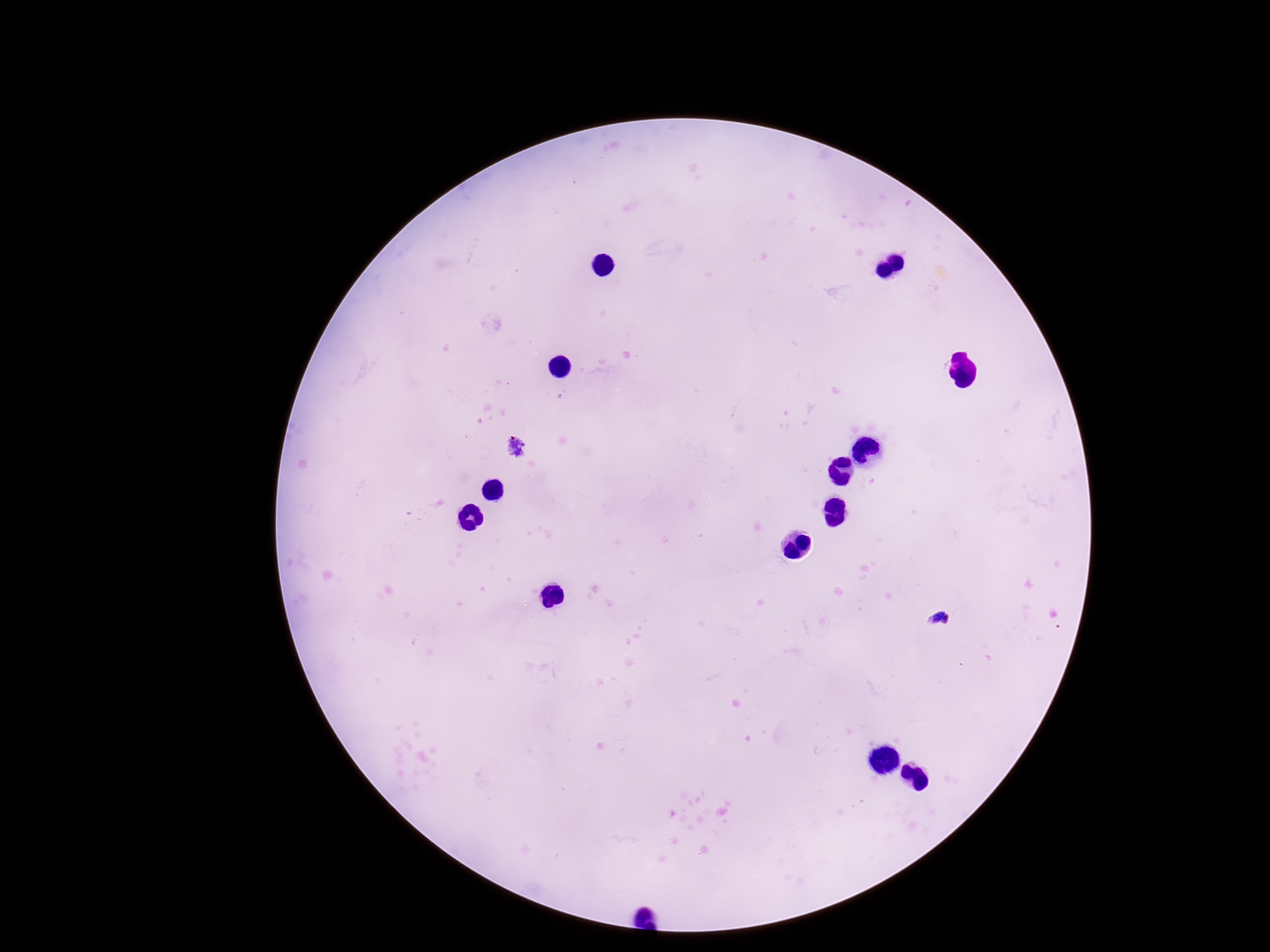 Approximate centers as (x, y) in pixels. Plasmodium parasite locations: (516, 447), (939, 621). Thick blood smear. 100x magnification. One field from this slide. Giemsa stain. Photographed through the microscope eyepiece with a smartphone camera. Image is 1270×952 pixels. Patient malaria status: positive.